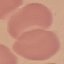
Summary:
  - Result: negative for malaria parasites
  - Capture: smartphone camera at the microscope eyepiece
  - Preparation: thin blood film
  - Stain: Giemsa
  - Image type: automatically extracted cell patch, resized to 64 × 64 pixels